Classify this cell by malaria status.
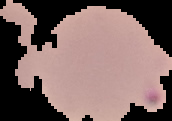
It is parasitized.

preparation = thin blood film
image size = 172×121 pixels
image type = cell region segmented out of the field of view; surrounding area masked to black